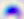

{
  "magnification": "400x",
  "modality": "micrograph",
  "identification": "Toxoplasma gondii"
}